Assess this cell for malaria.
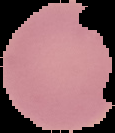

It is uninfected.

Summary:
  - Image type: segmented cell region with the area outside set to black
  - Preparation: thin blood film
  - Image size: 115×133 pixels